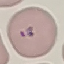 Malaria status: parasitized. Giemsa-stained preparation. Thin blood film. Cell patch, automatically extracted from a larger field of view and resized to 64 × 64 pixels. Acquired by smartphone through the microscope eyepiece.